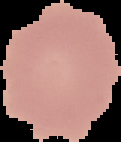

Summary:
  - Image type: segmented cell region on a black background
  - Image size: 121×142 pixels
  - Malaria status: uninfected
  - Preparation: thin blood smear